Classify this cell by malaria status.
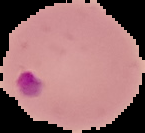

Parasitized.

image size = 145×133 pixels
preparation = thin blood film
image type = segmented cell region on a black background